Identify the blood parasite species.
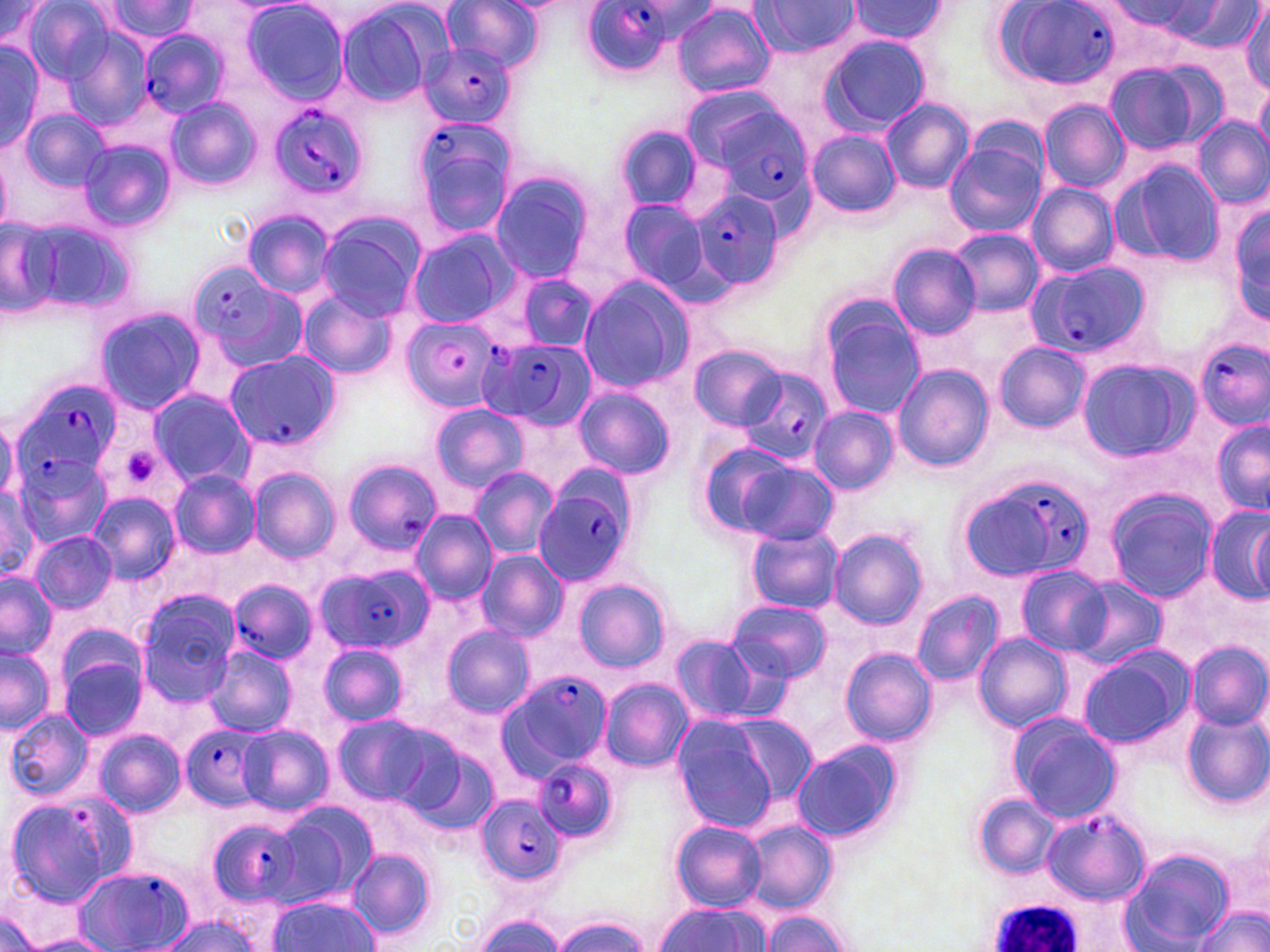
Plasmodium falciparum.

platelet_locations: 'approximate bounding boxes as (x1, y1, x2, y2) in pixels: (117, 446, 165, 491)'
magnification: 1000x
preparation: thin blood film
stain: May-Grünwald-Giemsa
uninfected_red_blood_cell_locations_subset: 'approximate bounding boxes as (x1, y1, x2, y2) in pixels: (440, 0, 543, 71), (93, 1, 200, 43), (238, 1, 350, 104), (845, 1, 949, 47), (1, 2, 56, 55), (747, 2, 863, 56), (1110, 2, 1223, 41), (23, 3, 117, 84), (333, 3, 442, 107), (672, 3, 775, 97), (1176, 4, 1267, 49), (1240, 4, 1270, 94), (56, 23, 155, 130), (818, 33, 931, 134), (0, 41, 51, 151), (1104, 59, 1216, 155), (1255, 80, 1270, 160), (165, 96, 259, 190), (881, 98, 974, 194), (1039, 100, 1129, 192), (19, 106, 111, 194), (1192, 116, 1270, 210), (613, 125, 703, 211), (807, 130, 900, 217), (77, 138, 177, 233), (944, 138, 1046, 239), (1116, 160, 1225, 265), (489, 172, 595, 284), (1026, 183, 1120, 277), (612, 196, 713, 299), (1229, 198, 1270, 326), (242, 208, 336, 299), (7, 213, 137, 322), (315, 213, 424, 321), (950, 228, 1043, 318), (405, 230, 518, 329), (887, 243, 982, 339), (514, 274, 599, 351), (576, 276, 697, 392), (297, 289, 398, 380), (818, 303, 926, 420), (94, 305, 206, 415), (993, 342, 1090, 432), (691, 344, 787, 430), (892, 365, 993, 473), (572, 386, 675, 480), (145, 387, 254, 488), (429, 403, 528, 495), (809, 407, 898, 493), (0, 414, 18, 503), (1212, 419, 1269, 516), (693, 437, 802, 537), (730, 458, 840, 545), (469, 467, 559, 557), (250, 469, 339, 562), (0, 470, 69, 570), (168, 470, 261, 558), (0, 486, 42, 582), (1103, 488, 1219, 603), (87, 491, 180, 583), (1203, 503, 1270, 607), (410, 509, 496, 604), (1251, 516, 1268, 602), (746, 525, 844, 613), (830, 529, 928, 629), (29, 531, 117, 612), (475, 550, 567, 643), (1014, 565, 1114, 656), (0, 572, 55, 658), (1066, 575, 1168, 669), (571, 577, 671, 672), (912, 589, 1004, 686), (135, 590, 242, 707), (727, 599, 831, 684), (440, 623, 535, 719), (668, 632, 772, 725), (974, 633, 1071, 733), (319, 642, 408, 727), (1186, 643, 1268, 730), (0, 644, 55, 732), (203, 644, 296, 737), (840, 646, 938, 746), (1076, 647, 1192, 749), (57, 649, 150, 741), (599, 678, 692, 771), (1180, 706, 1270, 806), (3, 709, 94, 801), (331, 713, 441, 806), (721, 713, 820, 806), (1007, 715, 1120, 823), (671, 716, 781, 832), (237, 724, 333, 816), (93, 728, 186, 818), (791, 739, 903, 844), (400, 741, 501, 837), (2, 790, 135, 907), (973, 794, 1060, 878), (273, 799, 379, 905), (1245, 809, 1270, 902), (671, 820, 767, 910), (741, 820, 838, 913), (1121, 847, 1233, 950), (346, 848, 437, 942), (266, 896, 377, 950), (1197, 903, 1268, 952), (652, 904, 771, 952), (0, 910, 45, 952), (469, 913, 571, 952), (759, 913, 855, 952), (155, 914, 264, 952), (551, 917, 651, 952), (27, 935, 116, 952)'
plasmodium_falciparum_infected_red_blood_cell_locations_subset: 'approximate bounding boxes as (x1, y1, x2, y2) in pixels: (998, 0, 1123, 84), (577, 3, 688, 73), (139, 28, 227, 120), (418, 42, 514, 127), (689, 89, 817, 209), (266, 104, 368, 202), (411, 114, 518, 237), (691, 188, 784, 289), (186, 259, 304, 366), (1030, 260, 1149, 359), (405, 317, 502, 409), (1195, 338, 1269, 429), (481, 339, 594, 429), (223, 352, 341, 452), (738, 367, 831, 464), (16, 378, 124, 479), (11, 447, 110, 545), (341, 458, 442, 555), (957, 466, 1105, 585), (532, 468, 639, 587), (315, 565, 432, 654), (228, 579, 320, 662), (496, 671, 610, 778), (181, 725, 267, 810), (531, 759, 618, 843), (475, 794, 568, 888), (1043, 810, 1148, 904), (206, 819, 303, 906), (70, 866, 191, 950)'
modality: optical microscopy
image_size: 1270×952 pixels
field_of_view: single
white_blood_cell_locations: 'approximate bounding boxes as (x1, y1, x2, y2) in pixels: (983, 900, 1084, 952)'